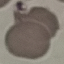
Result: no malaria parasites detected. Automatically extracted cell patch, resized to 64 × 64 pixels. Photographed with a smartphone camera at the microscope eyepiece. Thin blood smear. Giemsa stain.